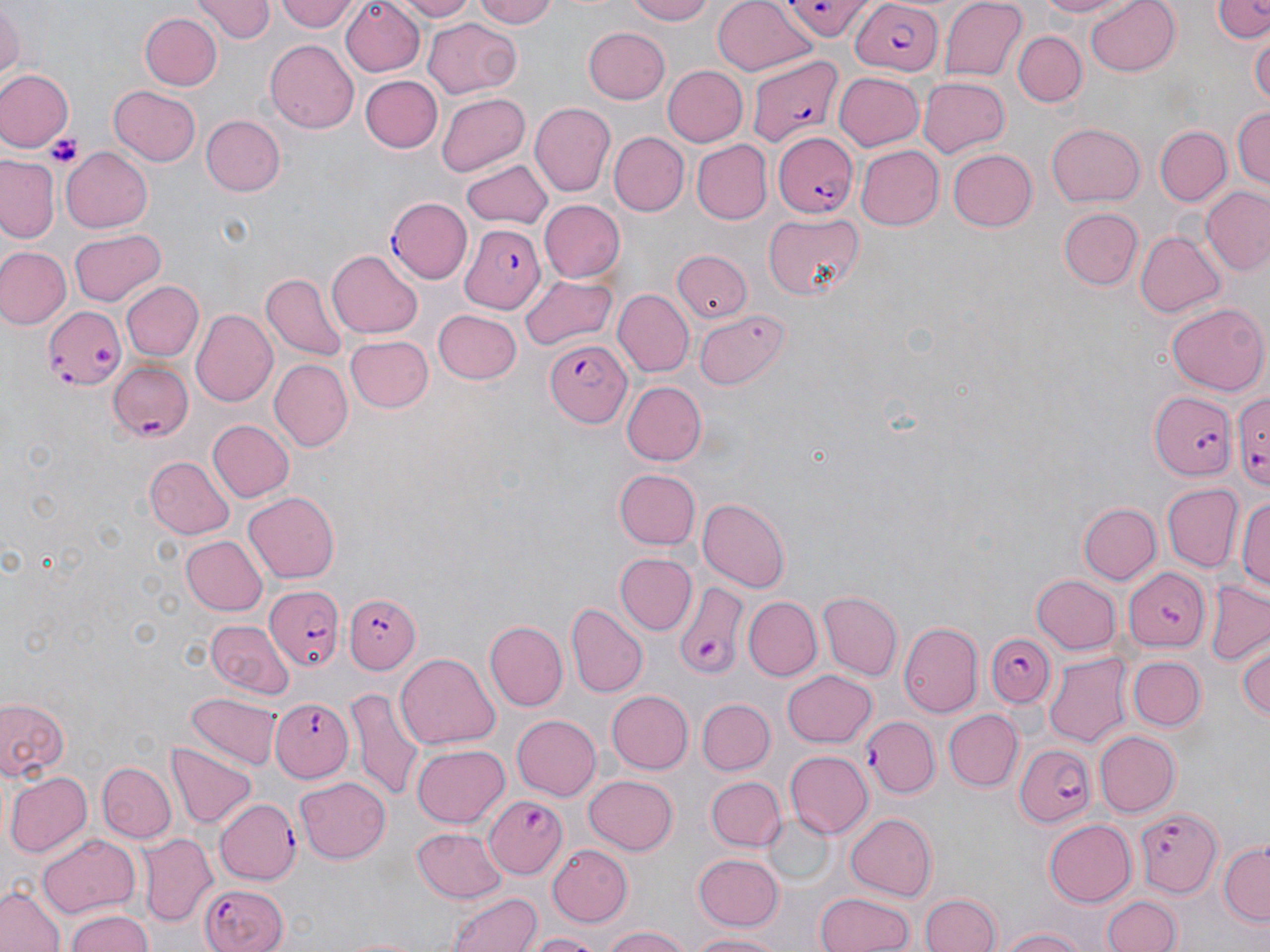
Summary:
  - Coordinate format: approximate bounding boxes as named x1/y1/x2/y2 corners in pixels
  - Uninfected red blood cell locations: (x1=195, y1=0, x2=274, y2=42), (x1=271, y1=0, x2=362, y2=34), (x1=389, y1=0, x2=479, y2=21), (x1=472, y1=0, x2=563, y2=28), (x1=625, y1=0, x2=718, y2=26), (x1=712, y1=0, x2=819, y2=78), (x1=940, y1=0, x2=1027, y2=83), (x1=1033, y1=0, x2=1135, y2=19), (x1=1086, y1=0, x2=1181, y2=75), (x1=1212, y1=0, x2=1270, y2=44), (x1=338, y1=1, x2=425, y2=74), (x1=0, y1=3, x2=22, y2=82), (x1=140, y1=12, x2=222, y2=91), (x1=423, y1=17, x2=521, y2=98), (x1=582, y1=27, x2=670, y2=105), (x1=1013, y1=29, x2=1087, y2=106), (x1=1250, y1=31, x2=1269, y2=112), (x1=264, y1=39, x2=359, y2=132), (x1=660, y1=64, x2=748, y2=147), (x1=0, y1=68, x2=73, y2=150), (x1=834, y1=71, x2=925, y2=151), (x1=360, y1=76, x2=442, y2=154), (x1=917, y1=76, x2=1010, y2=159), (x1=108, y1=85, x2=202, y2=167), (x1=436, y1=93, x2=529, y2=177), (x1=531, y1=102, x2=614, y2=198), (x1=1232, y1=104, x2=1270, y2=192), (x1=201, y1=116, x2=286, y2=196), (x1=1046, y1=121, x2=1146, y2=207), (x1=1156, y1=126, x2=1230, y2=206), (x1=609, y1=132, x2=687, y2=215), (x1=694, y1=141, x2=771, y2=225), (x1=853, y1=144, x2=942, y2=232), (x1=945, y1=147, x2=1036, y2=233), (x1=61, y1=148, x2=153, y2=232), (x1=1, y1=155, x2=61, y2=242), (x1=460, y1=161, x2=553, y2=230), (x1=1202, y1=187, x2=1270, y2=277), (x1=539, y1=199, x2=623, y2=283), (x1=1058, y1=206, x2=1143, y2=291), (x1=763, y1=211, x2=867, y2=300), (x1=70, y1=229, x2=167, y2=306), (x1=1135, y1=230, x2=1227, y2=318), (x1=0, y1=244, x2=71, y2=329), (x1=327, y1=249, x2=422, y2=338), (x1=673, y1=249, x2=750, y2=322), (x1=260, y1=273, x2=350, y2=363), (x1=519, y1=273, x2=617, y2=350), (x1=123, y1=281, x2=203, y2=361), (x1=617, y1=291, x2=693, y2=376), (x1=1166, y1=304, x2=1267, y2=397), (x1=694, y1=307, x2=790, y2=390), (x1=190, y1=308, x2=277, y2=408), (x1=433, y1=309, x2=522, y2=384), (x1=344, y1=335, x2=432, y2=412), (x1=268, y1=359, x2=352, y2=453), (x1=620, y1=382, x2=706, y2=466), (x1=206, y1=420, x2=293, y2=503), (x1=143, y1=454, x2=234, y2=538), (x1=614, y1=469, x2=699, y2=550), (x1=1162, y1=484, x2=1242, y2=572), (x1=1235, y1=487, x2=1270, y2=601), (x1=243, y1=491, x2=342, y2=583), (x1=698, y1=498, x2=789, y2=592), (x1=1077, y1=502, x2=1160, y2=583), (x1=183, y1=537, x2=267, y2=616), (x1=615, y1=552, x2=696, y2=634), (x1=1030, y1=575, x2=1119, y2=654), (x1=1204, y1=582, x2=1269, y2=665), (x1=818, y1=590, x2=902, y2=678), (x1=744, y1=596, x2=821, y2=679), (x1=569, y1=604, x2=646, y2=695), (x1=204, y1=620, x2=293, y2=695), (x1=485, y1=620, x2=568, y2=711), (x1=900, y1=621, x2=983, y2=716), (x1=1233, y1=635, x2=1270, y2=725), (x1=395, y1=652, x2=502, y2=749), (x1=1045, y1=652, x2=1131, y2=747), (x1=1127, y1=654, x2=1206, y2=732), (x1=781, y1=669, x2=878, y2=747), (x1=348, y1=684, x2=423, y2=803), (x1=690, y1=687, x2=848, y2=762), (x1=607, y1=690, x2=694, y2=773), (x1=186, y1=691, x2=280, y2=767), (x1=0, y1=695, x2=73, y2=783), (x1=698, y1=698, x2=774, y2=774), (x1=946, y1=709, x2=1022, y2=792), (x1=511, y1=714, x2=601, y2=801), (x1=1092, y1=730, x2=1180, y2=818), (x1=165, y1=742, x2=258, y2=829), (x1=410, y1=743, x2=509, y2=828), (x1=786, y1=750, x2=871, y2=836), (x1=96, y1=762, x2=176, y2=844), (x1=4, y1=771, x2=90, y2=857), (x1=583, y1=773, x2=678, y2=854), (x1=293, y1=775, x2=388, y2=863), (x1=706, y1=777, x2=784, y2=850), (x1=216, y1=798, x2=299, y2=883), (x1=845, y1=811, x2=937, y2=900), (x1=766, y1=813, x2=836, y2=885), (x1=1042, y1=818, x2=1136, y2=907), (x1=412, y1=826, x2=504, y2=903), (x1=139, y1=832, x2=216, y2=924), (x1=35, y1=833, x2=139, y2=917), (x1=549, y1=843, x2=636, y2=925), (x1=1219, y1=844, x2=1270, y2=926), (x1=691, y1=852, x2=784, y2=934), (x1=0, y1=882, x2=67, y2=952), (x1=445, y1=889, x2=544, y2=952), (x1=815, y1=891, x2=915, y2=952), (x1=919, y1=892, x2=1001, y2=952), (x1=1103, y1=893, x2=1181, y2=951), (x1=65, y1=907, x2=154, y2=952), (x1=597, y1=926, x2=694, y2=952), (x1=996, y1=927, x2=1092, y2=952), (x1=689, y1=930, x2=789, y2=951), (x1=524, y1=931, x2=607, y2=952), (x1=339, y1=933, x2=424, y2=952)
  - Platelet locations: (x1=45, y1=132, x2=84, y2=167)
  - Plasmodium falciparum-infected red blood cell locations: (x1=783, y1=0, x2=871, y2=37), (x1=848, y1=3, x2=944, y2=76), (x1=747, y1=56, x2=846, y2=152), (x1=771, y1=129, x2=860, y2=218), (x1=386, y1=199, x2=474, y2=283), (x1=461, y1=224, x2=547, y2=312), (x1=45, y1=304, x2=125, y2=393), (x1=546, y1=339, x2=633, y2=427), (x1=108, y1=360, x2=194, y2=442), (x1=1149, y1=390, x2=1237, y2=479), (x1=1233, y1=393, x2=1270, y2=485), (x1=1121, y1=569, x2=1210, y2=651), (x1=269, y1=586, x2=345, y2=671), (x1=671, y1=587, x2=749, y2=677), (x1=347, y1=593, x2=424, y2=674), (x1=987, y1=632, x2=1058, y2=705), (x1=269, y1=698, x2=352, y2=784), (x1=861, y1=717, x2=939, y2=798), (x1=1013, y1=743, x2=1094, y2=827), (x1=484, y1=796, x2=567, y2=879), (x1=1137, y1=806, x2=1222, y2=898), (x1=200, y1=881, x2=288, y2=952)
  - Slide-level diagnosis: Plasmodium falciparum
  - Field of view: single
  - Preparation: thin blood film
  - Modality: optical microscopy
  - Stain: May-Grünwald-Giemsa
  - Magnification: 1000x
  - Image size: 1270×952 pixels